Classify this cell by malaria status.
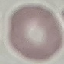
Uninfected.

image type = automatically extracted cell patch, resized to 64 × 64 pixels
capture = smartphone camera at the microscope eyepiece
preparation = thin blood smear
stain = Giemsa